Outline each Plasmodium malariae-infected red blood cell.
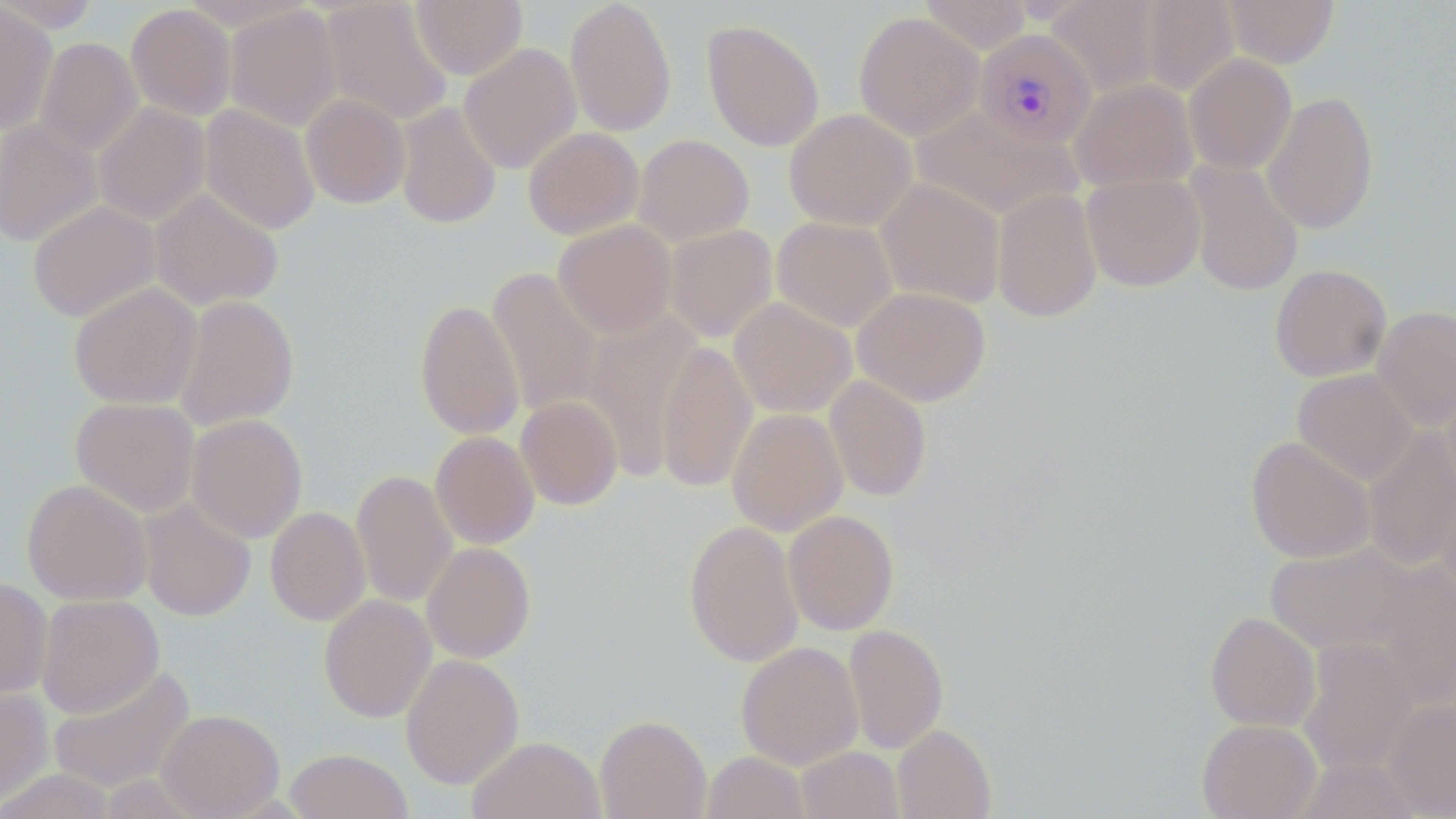

Approximate bounding boxes as named x1/y1/x2/y2 corners in pixels.
Plasmodium malariae-infected red blood cells: (x1=973, y1=29, x2=1097, y2=149).

{
  "slide_level_diagnosis": "Plasmodium malariae",
  "field_of_view": "one of a larger specimen",
  "modality": "light microscopy",
  "uninfected_red_blood_cell_locations": "approximate bounding boxes as named x1/y1/x2/y2 corners in pixels: (x1=0, y1=0, x2=103, y2=33), (x1=320, y1=0, x2=453, y2=125), (x1=411, y1=0, x2=527, y2=79), (x1=564, y1=0, x2=677, y2=137), (x1=917, y1=0, x2=1034, y2=54), (x1=1045, y1=0, x2=1164, y2=98), (x1=1139, y1=0, x2=1240, y2=97), (x1=1221, y1=0, x2=1340, y2=67), (x1=0, y1=1, x2=57, y2=134), (x1=125, y1=4, x2=237, y2=120), (x1=224, y1=5, x2=342, y2=132), (x1=853, y1=11, x2=983, y2=140), (x1=701, y1=19, x2=824, y2=151), (x1=36, y1=37, x2=142, y2=155), (x1=459, y1=43, x2=581, y2=174), (x1=1184, y1=53, x2=1297, y2=174), (x1=1069, y1=78, x2=1198, y2=191), (x1=1262, y1=90, x2=1379, y2=234), (x1=300, y1=94, x2=411, y2=209), (x1=395, y1=101, x2=502, y2=229), (x1=94, y1=103, x2=211, y2=225), (x1=200, y1=104, x2=320, y2=235), (x1=910, y1=106, x2=1080, y2=220), (x1=784, y1=108, x2=916, y2=230), (x1=0, y1=120, x2=102, y2=248), (x1=523, y1=127, x2=644, y2=240), (x1=633, y1=133, x2=755, y2=245), (x1=1184, y1=160, x2=1303, y2=297), (x1=1081, y1=173, x2=1206, y2=291), (x1=876, y1=179, x2=1005, y2=309), (x1=151, y1=189, x2=284, y2=310), (x1=992, y1=189, x2=1103, y2=322), (x1=27, y1=201, x2=160, y2=323), (x1=772, y1=216, x2=897, y2=332), (x1=553, y1=220, x2=676, y2=337), (x1=664, y1=224, x2=778, y2=343), (x1=1269, y1=264, x2=1392, y2=382), (x1=486, y1=267, x2=605, y2=419), (x1=68, y1=283, x2=202, y2=409), (x1=853, y1=287, x2=991, y2=406), (x1=173, y1=295, x2=300, y2=431), (x1=729, y1=297, x2=856, y2=417), (x1=414, y1=298, x2=525, y2=440), (x1=1372, y1=305, x2=1456, y2=431), (x1=581, y1=312, x2=705, y2=479), (x1=656, y1=339, x2=757, y2=493), (x1=1292, y1=368, x2=1417, y2=485), (x1=824, y1=375, x2=932, y2=502), (x1=1442, y1=381, x2=1456, y2=498), (x1=515, y1=396, x2=623, y2=510), (x1=70, y1=397, x2=199, y2=516), (x1=726, y1=408, x2=848, y2=535), (x1=186, y1=414, x2=308, y2=542), (x1=1363, y1=427, x2=1456, y2=572), (x1=430, y1=431, x2=539, y2=549), (x1=1245, y1=435, x2=1375, y2=563), (x1=351, y1=469, x2=457, y2=608), (x1=21, y1=478, x2=153, y2=605), (x1=1437, y1=479, x2=1456, y2=600), (x1=138, y1=498, x2=256, y2=621), (x1=265, y1=506, x2=370, y2=626), (x1=783, y1=509, x2=899, y2=635), (x1=683, y1=519, x2=803, y2=668), (x1=422, y1=542, x2=536, y2=663), (x1=1265, y1=543, x2=1417, y2=656), (x1=1371, y1=560, x2=1456, y2=711), (x1=0, y1=576, x2=52, y2=699), (x1=36, y1=594, x2=164, y2=718), (x1=318, y1=594, x2=436, y2=722), (x1=1205, y1=611, x2=1321, y2=732), (x1=844, y1=623, x2=948, y2=753), (x1=1297, y1=637, x2=1417, y2=775), (x1=736, y1=641, x2=863, y2=769), (x1=400, y1=653, x2=524, y2=789), (x1=47, y1=663, x2=196, y2=793), (x1=0, y1=685, x2=52, y2=808), (x1=1383, y1=699, x2=1456, y2=817), (x1=156, y1=709, x2=284, y2=819), (x1=595, y1=714, x2=711, y2=819), (x1=1197, y1=718, x2=1321, y2=819), (x1=892, y1=724, x2=996, y2=819), (x1=467, y1=736, x2=605, y2=819), (x1=797, y1=746, x2=904, y2=819), (x1=284, y1=748, x2=412, y2=819), (x1=702, y1=751, x2=810, y2=818), (x1=1294, y1=755, x2=1422, y2=818), (x1=0, y1=769, x2=118, y2=818)",
  "preparation": "thin blood film",
  "magnification": "1000x",
  "image_size": "1456×819 pixels",
  "stain": "May-Grünwald-Giemsa"
}